Point out each malaria parasite.
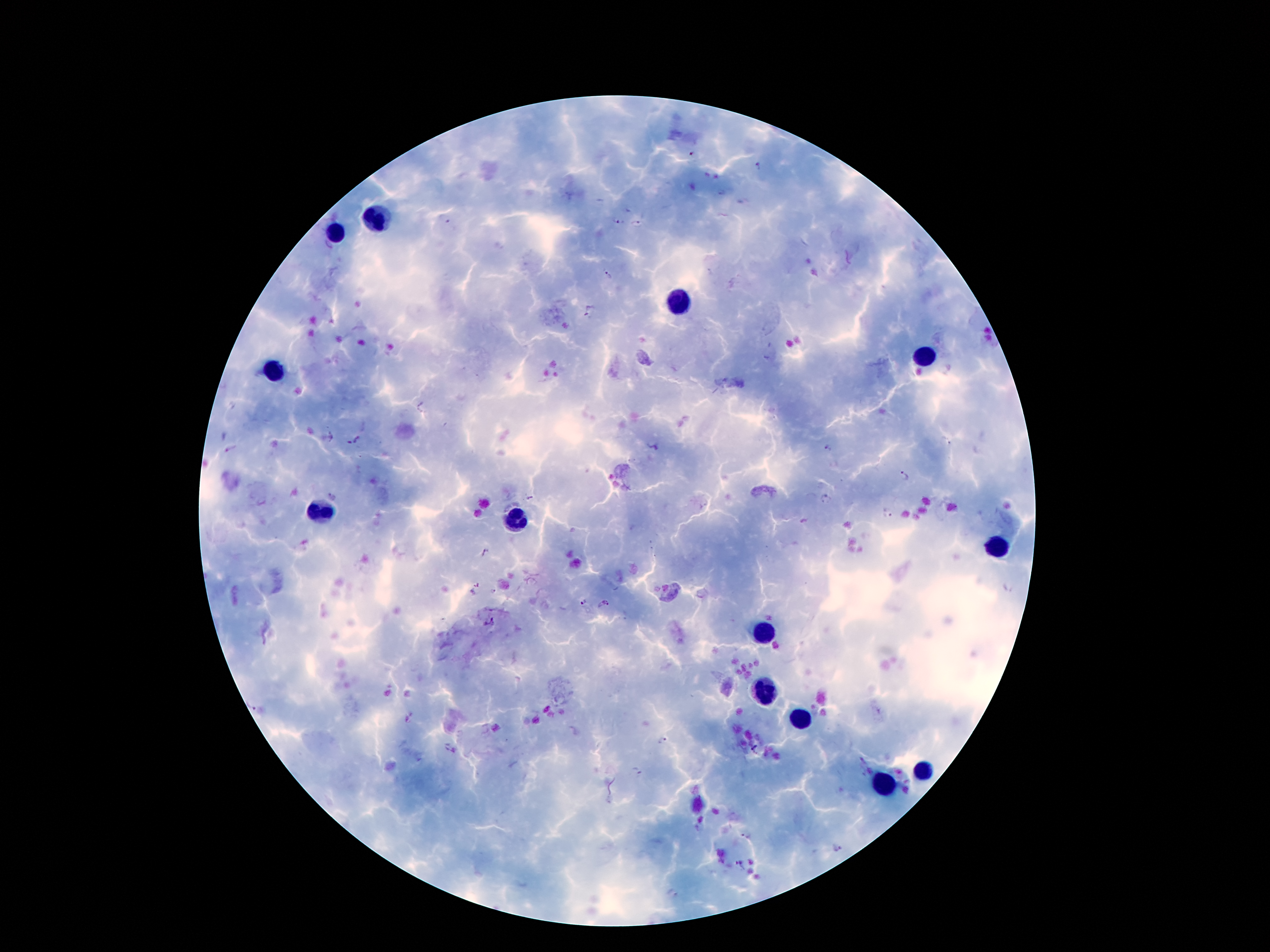

Approximate object centers, in pixels from the top-left corner.
Malaria parasites: (x=758, y=165), (x=444, y=219), (x=617, y=223), (x=638, y=224), (x=608, y=275), (x=590, y=313), (x=357, y=440), (x=349, y=444), (x=826, y=449), (x=231, y=450), (x=905, y=475), (x=335, y=495), (x=530, y=498), (x=825, y=498), (x=888, y=514), (x=485, y=553), (x=493, y=591), (x=608, y=601), (x=584, y=602), (x=488, y=622), (x=254, y=706), (x=663, y=741), (x=636, y=769), (x=747, y=837), (x=739, y=863).

Summary:
  - Leukocyte locations: (x=378, y=221), (x=334, y=234), (x=678, y=304), (x=926, y=356), (x=273, y=373), (x=323, y=513), (x=518, y=519), (x=997, y=550), (x=766, y=632), (x=766, y=692), (x=800, y=716), (x=924, y=769), (x=882, y=785)
  - Stain: Giemsa
  - Preparation: thick blood smear
  - Magnification: 100x
  - Patient malaria status: positive for Plasmodium falciparum
  - Capture: smartphone through the microscope eyepiece
  - Field of view: single
  - Image size: 1270×952 pixels